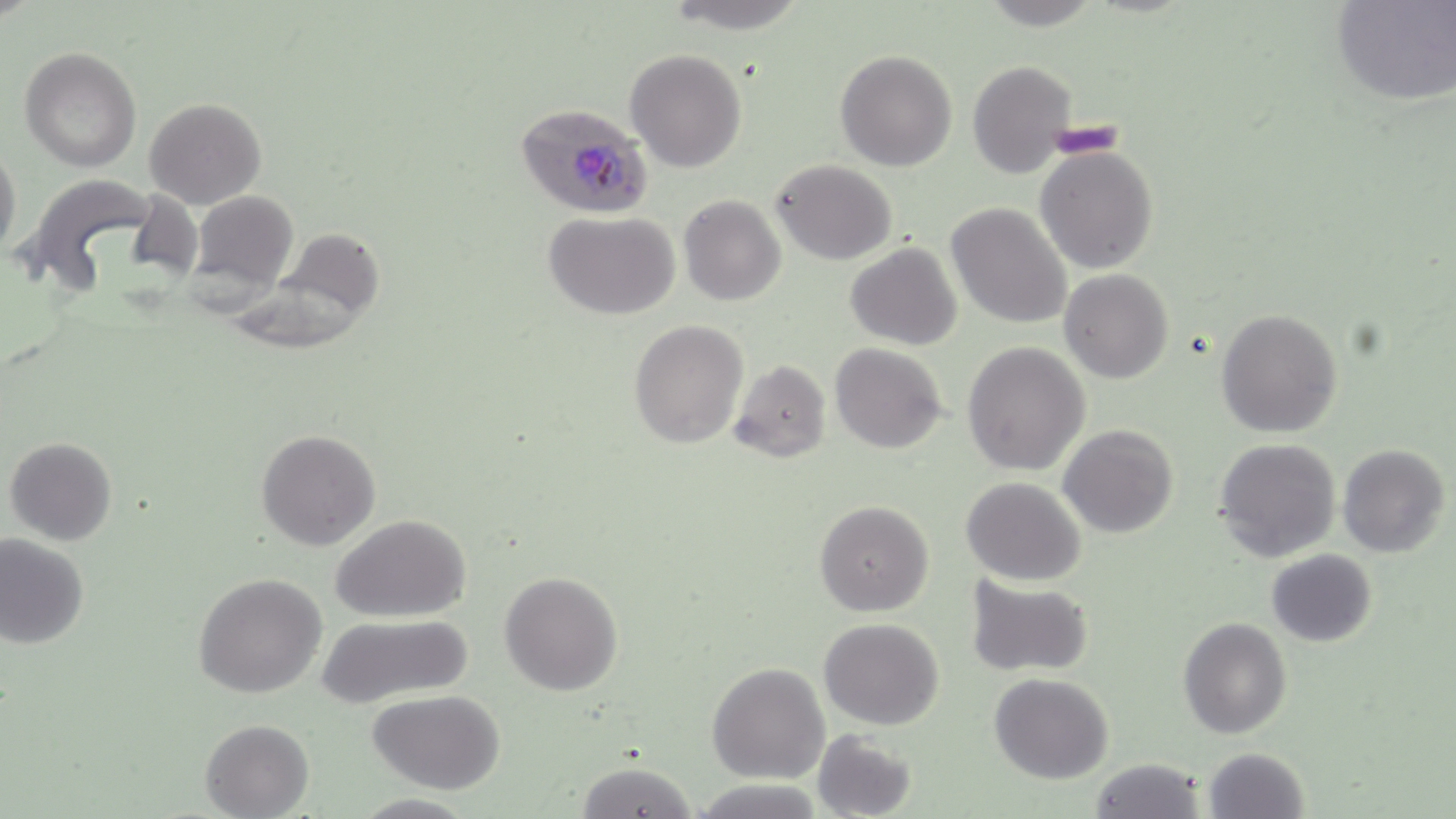

Summary:
  - Coordinate format: approximate bounding boxes as [x1, y1, x2, y2] in pixels
  - Uninfected red blood cell locations: [667, 0, 811, 31], [1331, 1, 1455, 107], [20, 47, 141, 172], [625, 49, 747, 172], [835, 50, 958, 171], [968, 60, 1078, 178], [144, 97, 266, 208], [0, 144, 22, 266], [1035, 145, 1158, 274], [769, 159, 897, 265], [26, 175, 158, 286], [188, 191, 299, 293], [679, 196, 785, 307], [946, 202, 1073, 332], [543, 212, 682, 320], [846, 244, 961, 349], [1060, 268, 1174, 384], [1216, 308, 1343, 439], [628, 319, 748, 449], [962, 342, 1090, 476], [830, 343, 947, 454], [728, 360, 832, 462], [1060, 423, 1178, 538], [255, 428, 381, 549], [4, 436, 119, 545], [1213, 437, 1343, 562], [1338, 444, 1449, 559], [961, 477, 1087, 586], [815, 500, 933, 616], [332, 515, 471, 622], [0, 534, 89, 648], [1266, 549, 1376, 647], [499, 570, 622, 695], [194, 571, 325, 699], [965, 576, 1093, 676], [312, 612, 474, 711], [1178, 616, 1291, 739], [818, 618, 945, 730], [708, 663, 829, 784], [989, 673, 1113, 785], [368, 690, 507, 793], [201, 719, 313, 818], [811, 729, 917, 819], [1202, 747, 1310, 819], [1087, 756, 1206, 819], [574, 760, 697, 818], [693, 778, 822, 817]
  - Plasmodium falciparum-infected red blood cell locations: [514, 104, 653, 220]
  - Slide-level diagnosis: Plasmodium falciparum
  - Field of view: one of a larger specimen
  - Modality: light microscopy
  - Preparation: thin blood smear
  - Image size: 1456×819 pixels
  - Stain: May-Grünwald-Giemsa
  - Magnification: 1000x